Locate and identify every blood parasite.
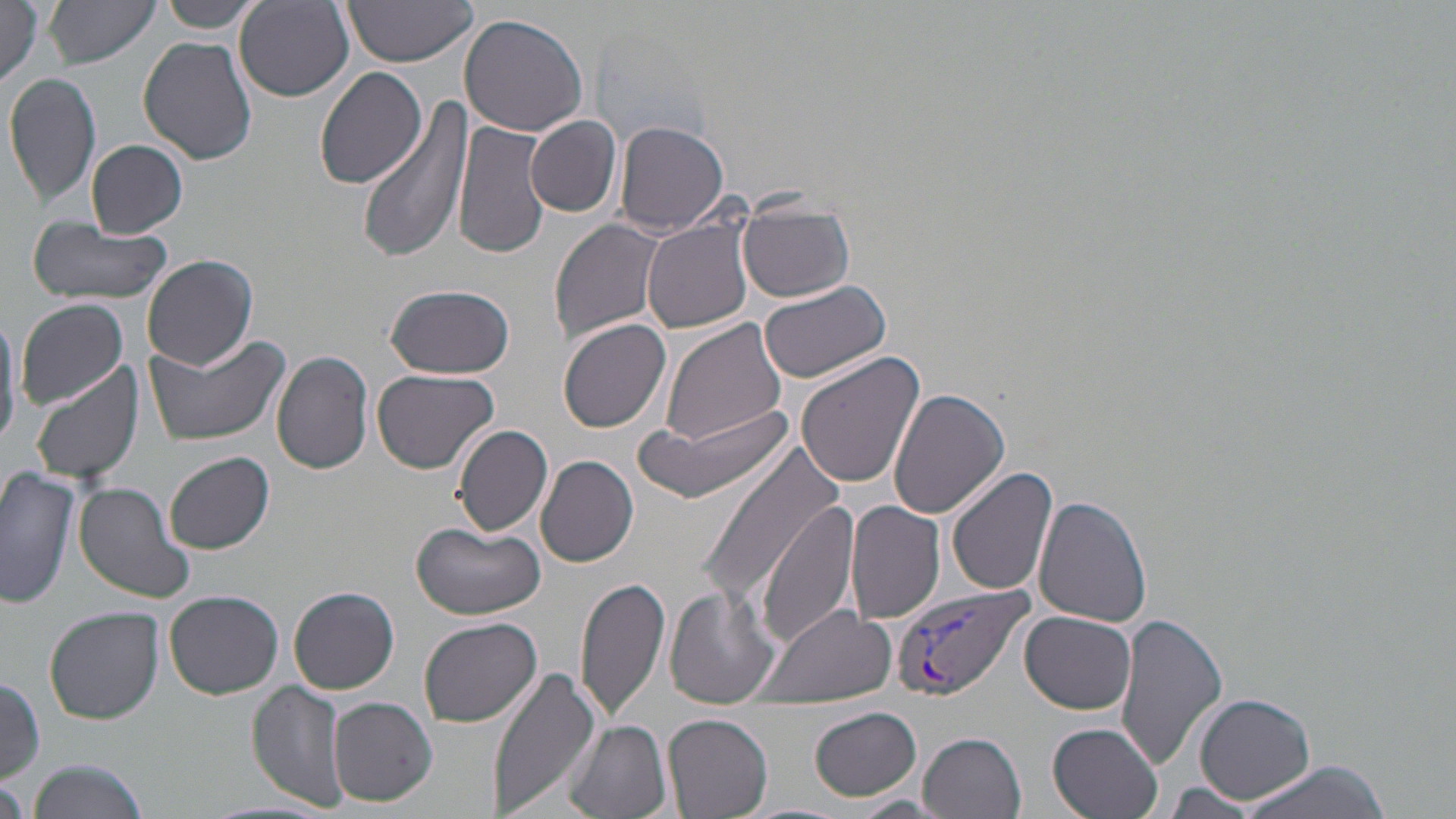
Approximate bounding boxes as named x1/y1/x2/y2 corners in pixels.
Plasmodium vivax-infected red blood cells: (x1=892, y1=583, x2=1032, y2=700).
No Plasmodium falciparum, Plasmodium ovale, Plasmodium malariae, Babesia divergens, or Trypanosoma brucei observed.

Uninfected red blood cell locations: (x1=0, y1=0, x2=48, y2=88), (x1=44, y1=0, x2=160, y2=69), (x1=159, y1=0, x2=264, y2=32), (x1=342, y1=1, x2=480, y2=67), (x1=233, y1=2, x2=354, y2=101), (x1=458, y1=12, x2=588, y2=137), (x1=138, y1=36, x2=258, y2=166), (x1=313, y1=66, x2=425, y2=189), (x1=5, y1=71, x2=102, y2=207), (x1=358, y1=99, x2=471, y2=262), (x1=527, y1=116, x2=622, y2=217), (x1=453, y1=118, x2=552, y2=261), (x1=612, y1=120, x2=730, y2=238), (x1=84, y1=140, x2=188, y2=238), (x1=737, y1=202, x2=855, y2=303), (x1=642, y1=218, x2=754, y2=333), (x1=25, y1=219, x2=173, y2=304), (x1=549, y1=219, x2=669, y2=343), (x1=143, y1=254, x2=258, y2=369), (x1=757, y1=279, x2=893, y2=384), (x1=383, y1=283, x2=515, y2=380), (x1=16, y1=298, x2=128, y2=407), (x1=558, y1=317, x2=672, y2=432), (x1=658, y1=318, x2=788, y2=449), (x1=143, y1=331, x2=292, y2=446), (x1=272, y1=349, x2=374, y2=474), (x1=794, y1=352, x2=927, y2=490), (x1=28, y1=362, x2=143, y2=484), (x1=371, y1=368, x2=500, y2=475), (x1=889, y1=387, x2=1011, y2=520), (x1=640, y1=411, x2=790, y2=504), (x1=453, y1=423, x2=553, y2=538), (x1=697, y1=441, x2=847, y2=612), (x1=165, y1=450, x2=274, y2=553), (x1=537, y1=455, x2=639, y2=567), (x1=945, y1=465, x2=1058, y2=597), (x1=0, y1=467, x2=81, y2=612), (x1=75, y1=482, x2=196, y2=603), (x1=1035, y1=495, x2=1154, y2=628), (x1=755, y1=499, x2=862, y2=646), (x1=847, y1=501, x2=946, y2=624), (x1=411, y1=521, x2=546, y2=621), (x1=574, y1=574, x2=671, y2=725), (x1=585, y1=584, x2=753, y2=716), (x1=287, y1=585, x2=399, y2=694), (x1=663, y1=586, x2=781, y2=709), (x1=163, y1=590, x2=283, y2=699), (x1=756, y1=604, x2=896, y2=705), (x1=45, y1=606, x2=163, y2=724), (x1=1019, y1=610, x2=1137, y2=715), (x1=1115, y1=611, x2=1230, y2=771), (x1=437, y1=616, x2=571, y2=794), (x1=418, y1=617, x2=542, y2=729), (x1=486, y1=664, x2=604, y2=819), (x1=0, y1=675, x2=46, y2=781), (x1=247, y1=682, x2=349, y2=811), (x1=1194, y1=692, x2=1315, y2=804), (x1=328, y1=695, x2=437, y2=807), (x1=808, y1=707, x2=922, y2=800), (x1=663, y1=712, x2=775, y2=818), (x1=563, y1=720, x2=672, y2=819), (x1=1047, y1=722, x2=1165, y2=819), (x1=920, y1=731, x2=1026, y2=817), (x1=1226, y1=759, x2=1398, y2=819), (x1=23, y1=760, x2=151, y2=819), (x1=1, y1=775, x2=28, y2=819), (x1=1157, y1=783, x2=1266, y2=817), (x1=849, y1=795, x2=950, y2=816). Slide-level diagnosis: Plasmodium vivax. May-Grünwald-Giemsa-stained preparation. Single field of view. 1000x magnification. Optical microscopy. Image is 1456×819 pixels. Thin blood film.